Comment on the morphology of the red blood cells.
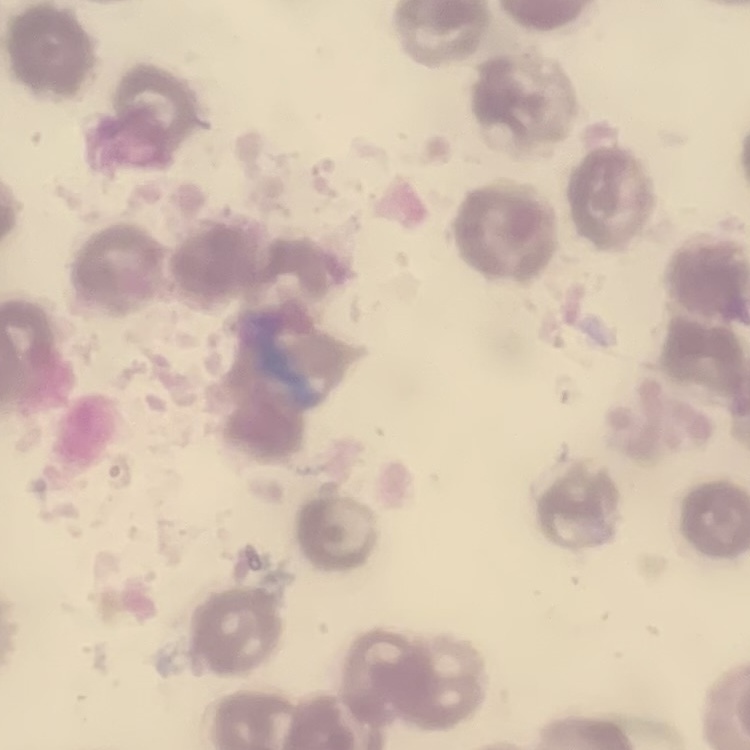

They show no rouleaux formation.

Summary:
  - Preparation: thin peripheral smear
  - Stain: Field's or Giemsa
  - Image type: square crop of a larger photomicrograph